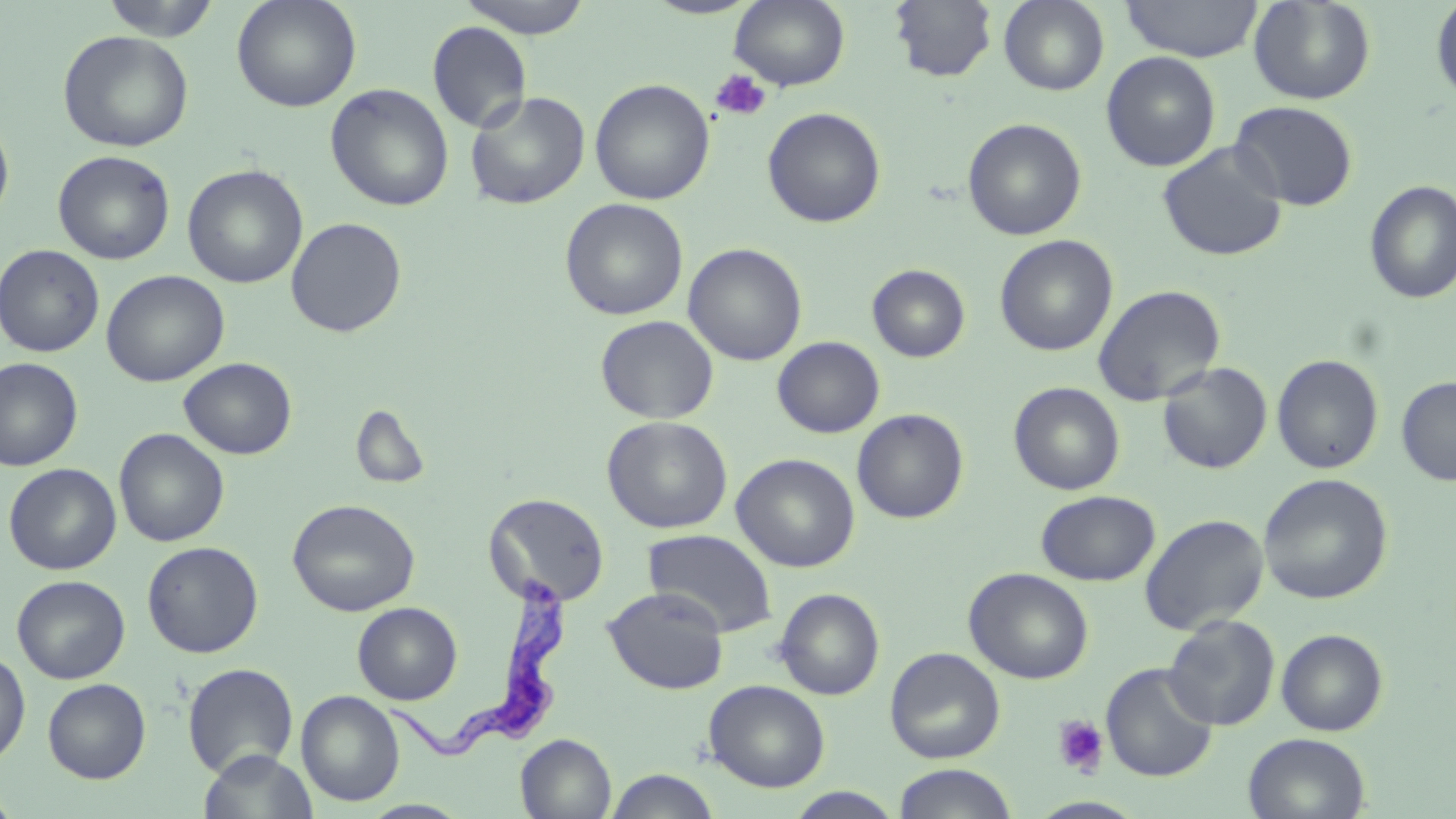 Approximate bounding boxes as named x1/y1/x2/y2 corners in pixels. Trypanosoma brucei locations: (x1=383, y1=575, x2=572, y2=762). Uninfected red blood cell locations: (x1=99, y1=0, x2=222, y2=40), (x1=231, y1=0, x2=361, y2=112), (x1=457, y1=0, x2=594, y2=38), (x1=729, y1=0, x2=850, y2=91), (x1=889, y1=0, x2=998, y2=82), (x1=999, y1=0, x2=1109, y2=95), (x1=1120, y1=0, x2=1264, y2=62), (x1=1248, y1=0, x2=1376, y2=105), (x1=1430, y1=0, x2=1456, y2=105), (x1=427, y1=21, x2=532, y2=133), (x1=58, y1=30, x2=194, y2=152), (x1=1101, y1=51, x2=1221, y2=171), (x1=589, y1=78, x2=715, y2=205), (x1=325, y1=83, x2=454, y2=211), (x1=465, y1=91, x2=590, y2=210), (x1=1229, y1=100, x2=1358, y2=211), (x1=762, y1=107, x2=886, y2=228), (x1=0, y1=114, x2=15, y2=227), (x1=962, y1=117, x2=1087, y2=241), (x1=1156, y1=142, x2=1288, y2=262), (x1=53, y1=150, x2=175, y2=265), (x1=51, y1=158, x2=306, y2=270), (x1=183, y1=164, x2=308, y2=288), (x1=1364, y1=179, x2=1456, y2=304), (x1=560, y1=198, x2=688, y2=321), (x1=285, y1=216, x2=407, y2=338), (x1=994, y1=234, x2=1118, y2=356), (x1=683, y1=243, x2=807, y2=366), (x1=0, y1=244, x2=105, y2=357), (x1=867, y1=264, x2=970, y2=362), (x1=101, y1=270, x2=230, y2=387), (x1=1092, y1=284, x2=1226, y2=406), (x1=595, y1=315, x2=719, y2=424), (x1=772, y1=336, x2=885, y2=438), (x1=1271, y1=354, x2=1383, y2=474), (x1=0, y1=357, x2=83, y2=471), (x1=178, y1=357, x2=297, y2=460), (x1=1157, y1=362, x2=1272, y2=474), (x1=1396, y1=376, x2=1456, y2=486), (x1=1008, y1=381, x2=1125, y2=495), (x1=353, y1=407, x2=430, y2=489), (x1=851, y1=408, x2=969, y2=523), (x1=602, y1=415, x2=732, y2=533), (x1=114, y1=428, x2=230, y2=547), (x1=731, y1=453, x2=860, y2=572), (x1=3, y1=462, x2=121, y2=575), (x1=1258, y1=473, x2=1393, y2=605), (x1=1035, y1=490, x2=1160, y2=586), (x1=483, y1=492, x2=610, y2=607), (x1=287, y1=498, x2=421, y2=616), (x1=1139, y1=513, x2=1269, y2=635), (x1=644, y1=528, x2=777, y2=637), (x1=142, y1=541, x2=264, y2=658), (x1=964, y1=567, x2=1094, y2=685), (x1=12, y1=575, x2=130, y2=683), (x1=602, y1=588, x2=729, y2=694), (x1=774, y1=588, x2=885, y2=700), (x1=352, y1=602, x2=462, y2=704), (x1=1163, y1=614, x2=1280, y2=730), (x1=1276, y1=628, x2=1388, y2=736), (x1=885, y1=647, x2=1005, y2=763), (x1=0, y1=650, x2=31, y2=765), (x1=182, y1=662, x2=298, y2=778), (x1=1101, y1=662, x2=1219, y2=782), (x1=42, y1=678, x2=151, y2=783), (x1=704, y1=679, x2=830, y2=792), (x1=296, y1=690, x2=405, y2=807), (x1=516, y1=733, x2=616, y2=819), (x1=1243, y1=733, x2=1371, y2=819), (x1=198, y1=749, x2=318, y2=819), (x1=892, y1=763, x2=1019, y2=819), (x1=604, y1=769, x2=721, y2=819), (x1=0, y1=787, x2=21, y2=819), (x1=786, y1=787, x2=904, y2=818), (x1=1028, y1=796, x2=1147, y2=818), (x1=359, y1=800, x2=472, y2=818). Platelet locations: (x1=710, y1=69, x2=772, y2=122), (x1=1052, y1=714, x2=1109, y2=776). Slide-level diagnosis: Trypanosoma brucei. May-Grünwald-Giemsa stain. Thin blood smear. Single field of view. Light microscopy. Captured at 1000x magnification. Image is 1456×819 pixels.